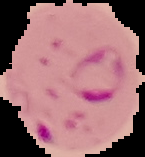

Summary:
  - Result: Plasmodium parasites detected
  - Preparation: thin blood smear
  - Image type: segmented cell region on a black background
  - Image size: 145×157 pixels